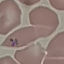
Malaria status: parasitized. Giemsa stain. Cell patch, automatically extracted from a larger field of view and resized to 64 × 64 pixels. Thin smear of blood. Acquired by smartphone through the microscope eyepiece.